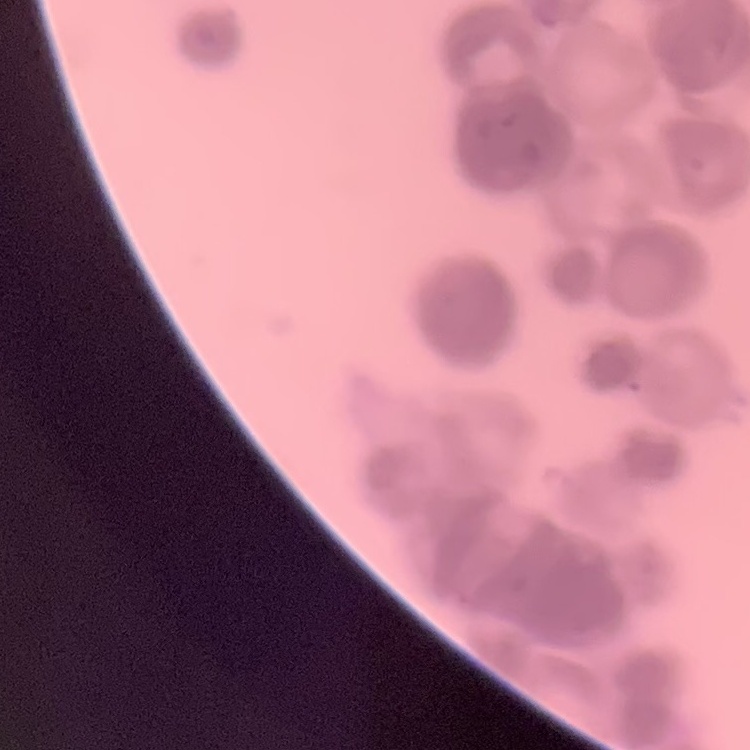

The erythrocytes show rouleaux formation. Field's or Giemsa stain. Thin blood smear. Square crop of a larger photomicrograph.